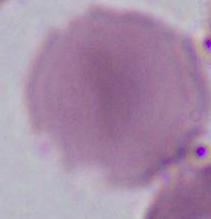

modality = photomicrograph
magnification = 1000x
identification = red blood cell